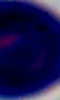

Summary:
  - Magnification: 1000x
  - Modality: micrograph
  - Identification: white blood cell